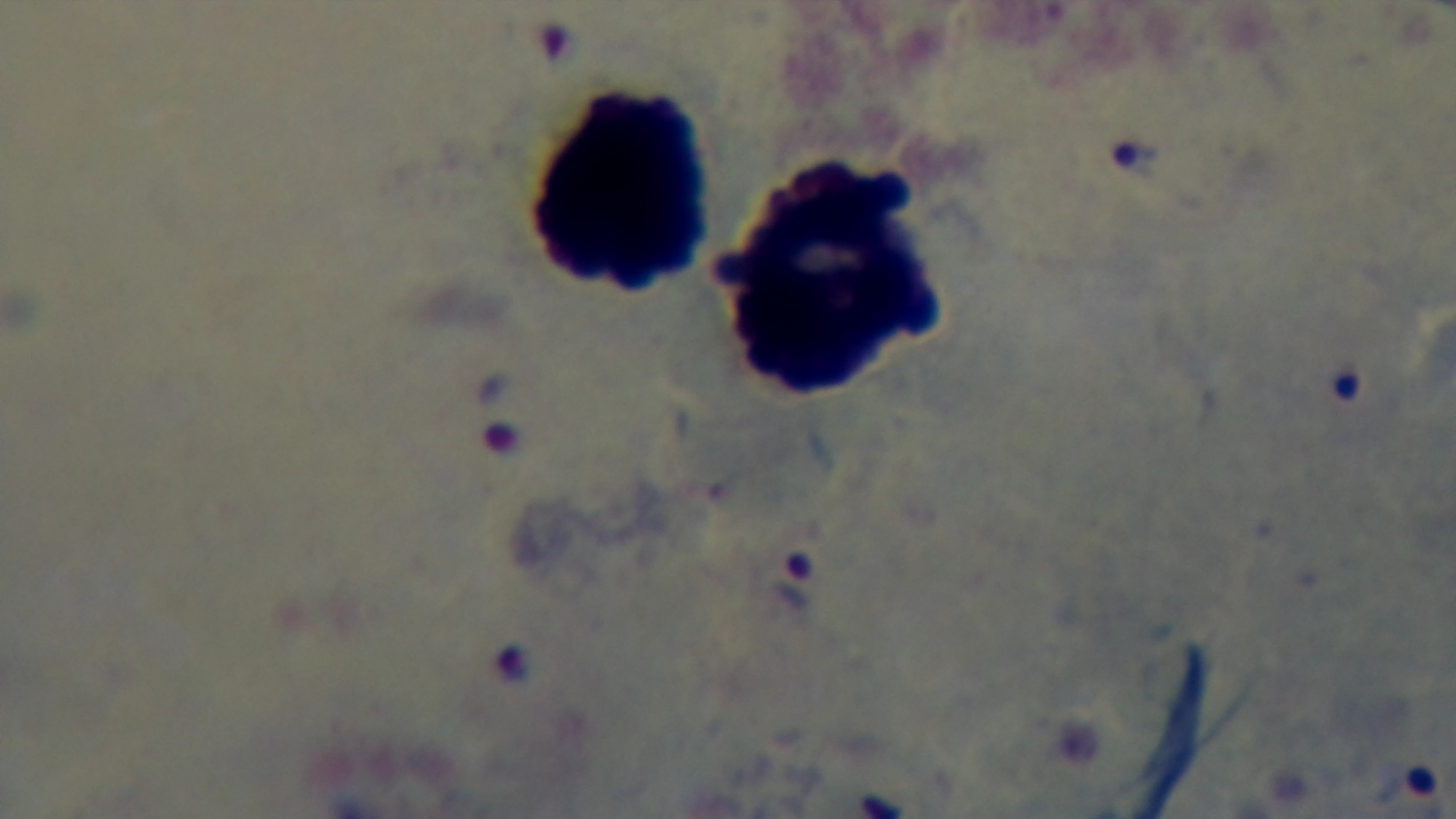

100x oil-immersion objective. Malaria status: infected. Captured with a mounted 4K digital camera. Preparation: thick smear. Single field of view. Photomicrograph. Giemsa-stained.